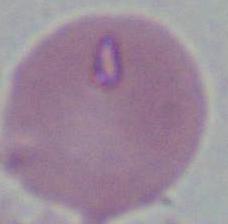
{
  "magnification": "1000x",
  "modality": "micrograph",
  "identification": "red blood cell"
}